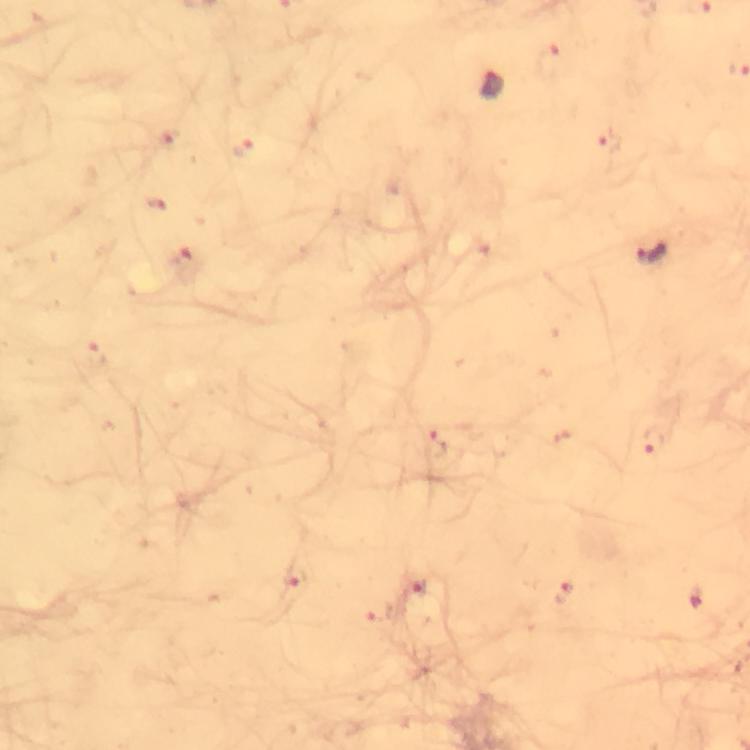
Approximate centers as [x, y] in pixels. Malaria parasite locations: [493, 83], [608, 141], [243, 148], [154, 204], [650, 254], [654, 442], [432, 446], [294, 580], [416, 589], [563, 594]. Immersion oil applied. At 100x magnification. Thick blood film. Photographed with a smartphone mounted on the microscope. Cropped region of a single field of view. Giemsa stain. From a diagnostic examination for malaria. Image is 750×750 pixels.